Locate every Plasmodium parasite.
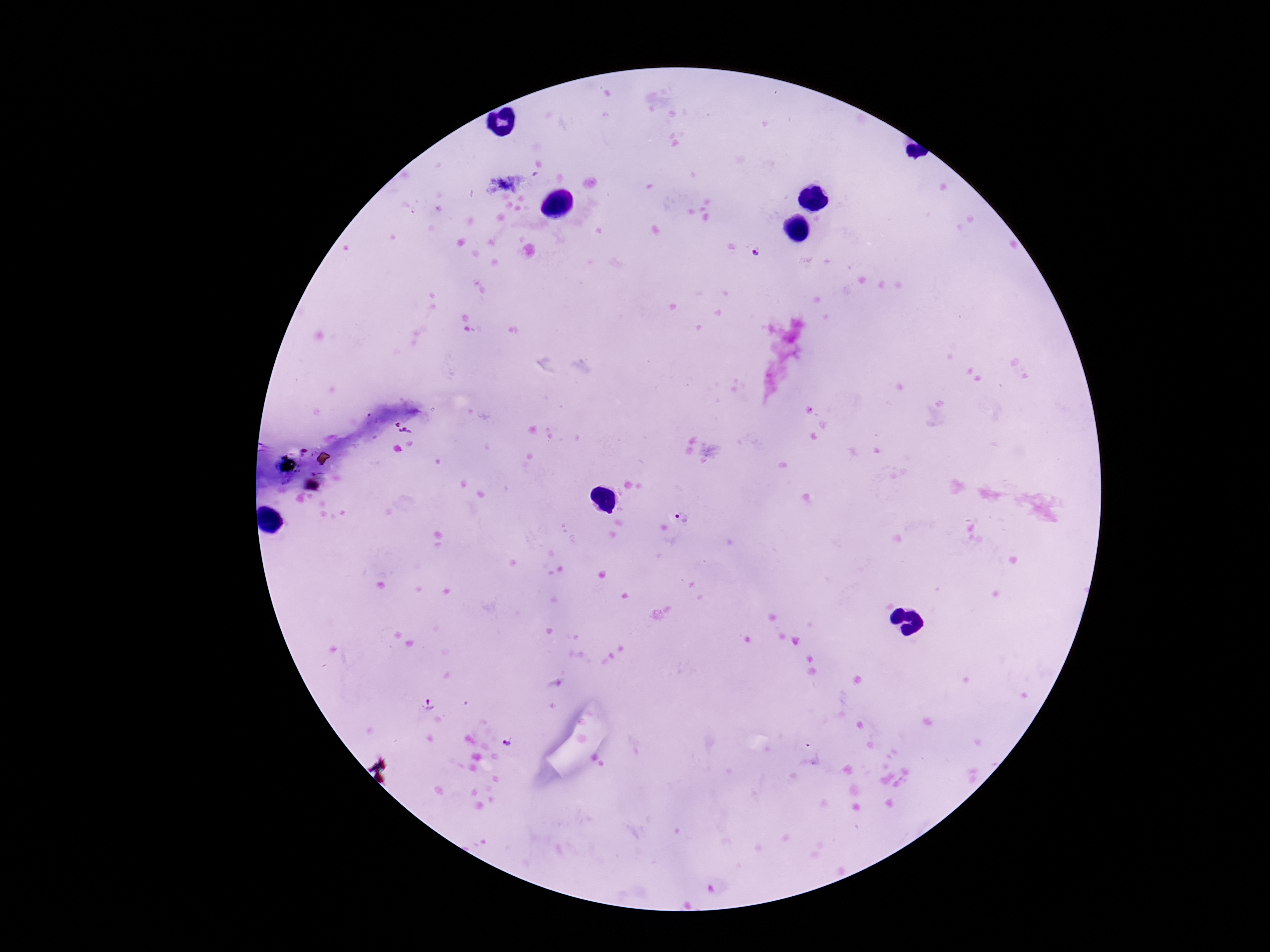
Approximate object centers, in pixels from the top-left corner.
Plasmodium parasites: (x=753, y=254), (x=406, y=432), (x=683, y=518).

Summary:
  - Field of view: one from this slide
  - Image size: 1270×952 pixels
  - Patient malaria status: positive
  - Preparation: thick blood smear
  - Capture: smartphone camera through the microscope eyepiece
  - Stain: Giemsa
  - Magnification: 100x